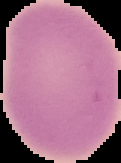 From a thin blood smear. Result: no malaria parasites detected. Image is 121×163 pixels. The area outside the segmented cell region is set to black.